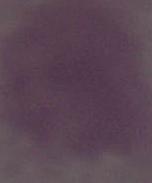
identification: red blood cell
magnification: 1000x
modality: photomicrograph